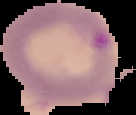

image type = segmented cell region on a black background
preparation = thin blood film
image size = 136×115 pixels
malaria status = parasitized